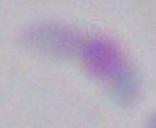
Summary:
  - Identification: Toxoplasma gondii
  - Modality: micrograph
  - Magnification: 1000x